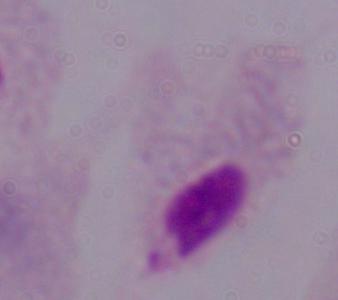

Summary:
  - Modality: photomicrograph
  - Magnification: 1000x
  - Identification: trichomonad